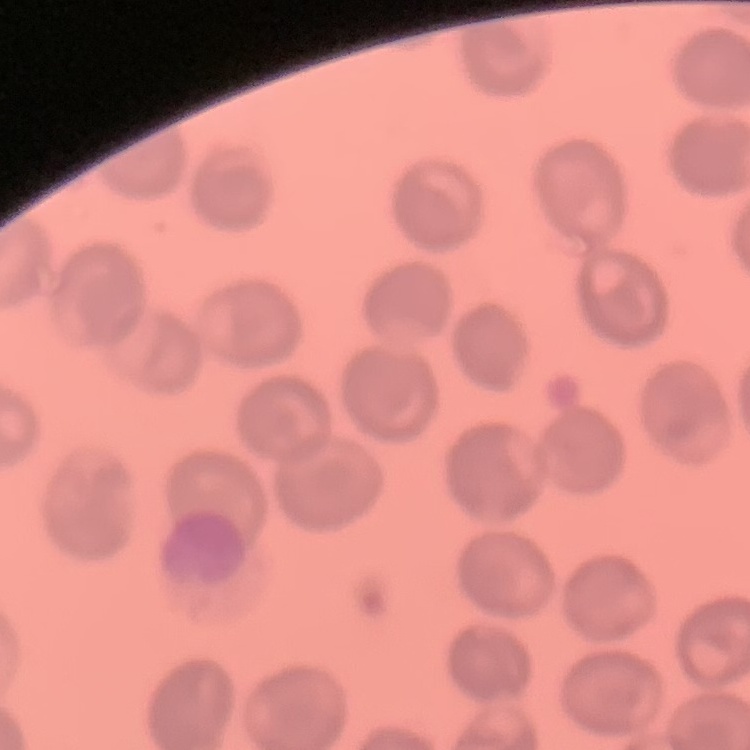
Summary:
  - Erythrocyte morphology: no rouleaux formation
  - Stain: Field's or Giemsa
  - Preparation: thin blood film
  - Image type: one tile cut from a larger photomicrograph